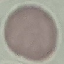
malaria status = uninfected
stain = Giemsa
preparation = thin smear
image type = automatically extracted cell patch, resized to 64 × 64 pixels
capture = smartphone through the microscope eyepiece